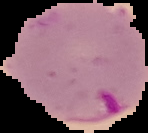 Malaria status: parasitized. Cell region segmented out of the field of view; the surrounding area is masked to black. From a thin blood film. Image is 148×133 pixels.